Report the malaria status of this cell.
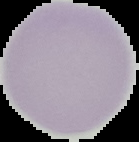

It is uninfected.

From a thin blood film. Image is 139×142 pixels. Cell region segmented out of the field of view; the surrounding area is masked to black.